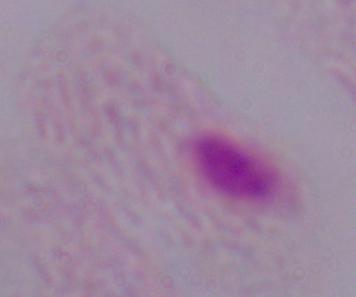
Summary:
  - Modality: micrograph
  - Magnification: 1000x
  - Identification: trichomonad